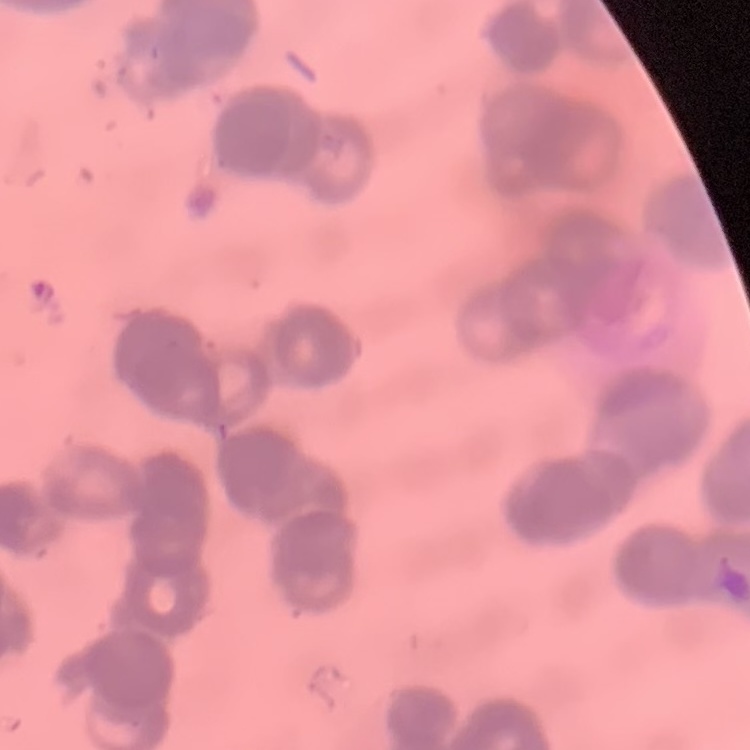

Summary:
  - Erythrocyte morphology: rouleaux formation
  - Stain: Field's or Giemsa
  - Image type: one tile cut from a larger photomicrograph
  - Preparation: thin peripheral smear